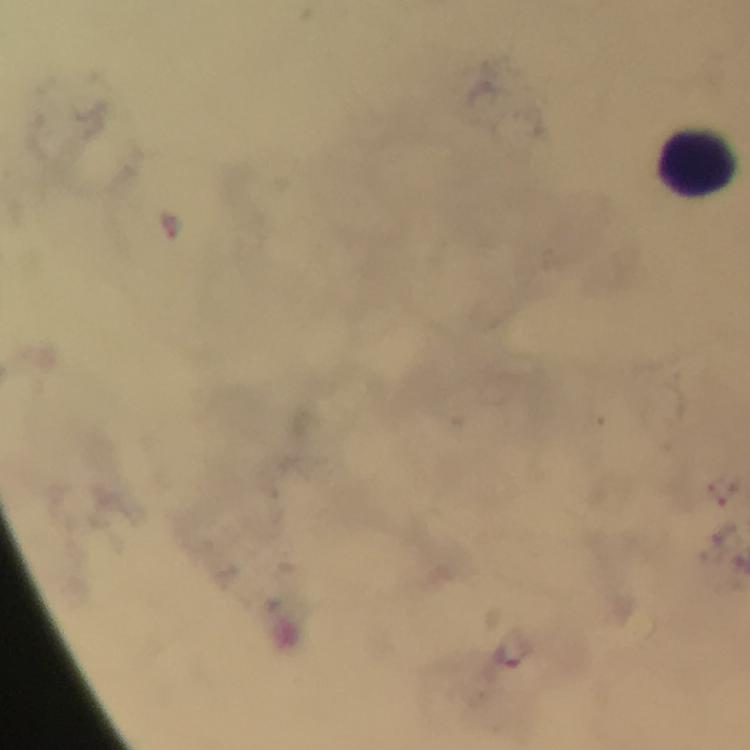
context = from a malaria diagnostic workup
leukocyte locations = approximate centers as (x, y) in pixels: (699, 159)
stain = Giemsa
preparation = thick blood film
capture = smartphone camera through the microscope
image size = 750×750 pixels
immersion oil = applied
cropped from = one field of view
malaria parasites = none detected
magnification = 100x